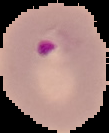
result: Plasmodium parasites detected
image_type: segmented cell region on a black background
preparation: thin blood smear
image_size: 109×133 pixels